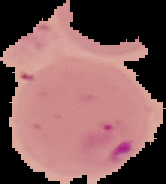 From a thin blood smear. Image is 166×184 pixels. Segmented cell region on a black background. Malaria status: parasitized.